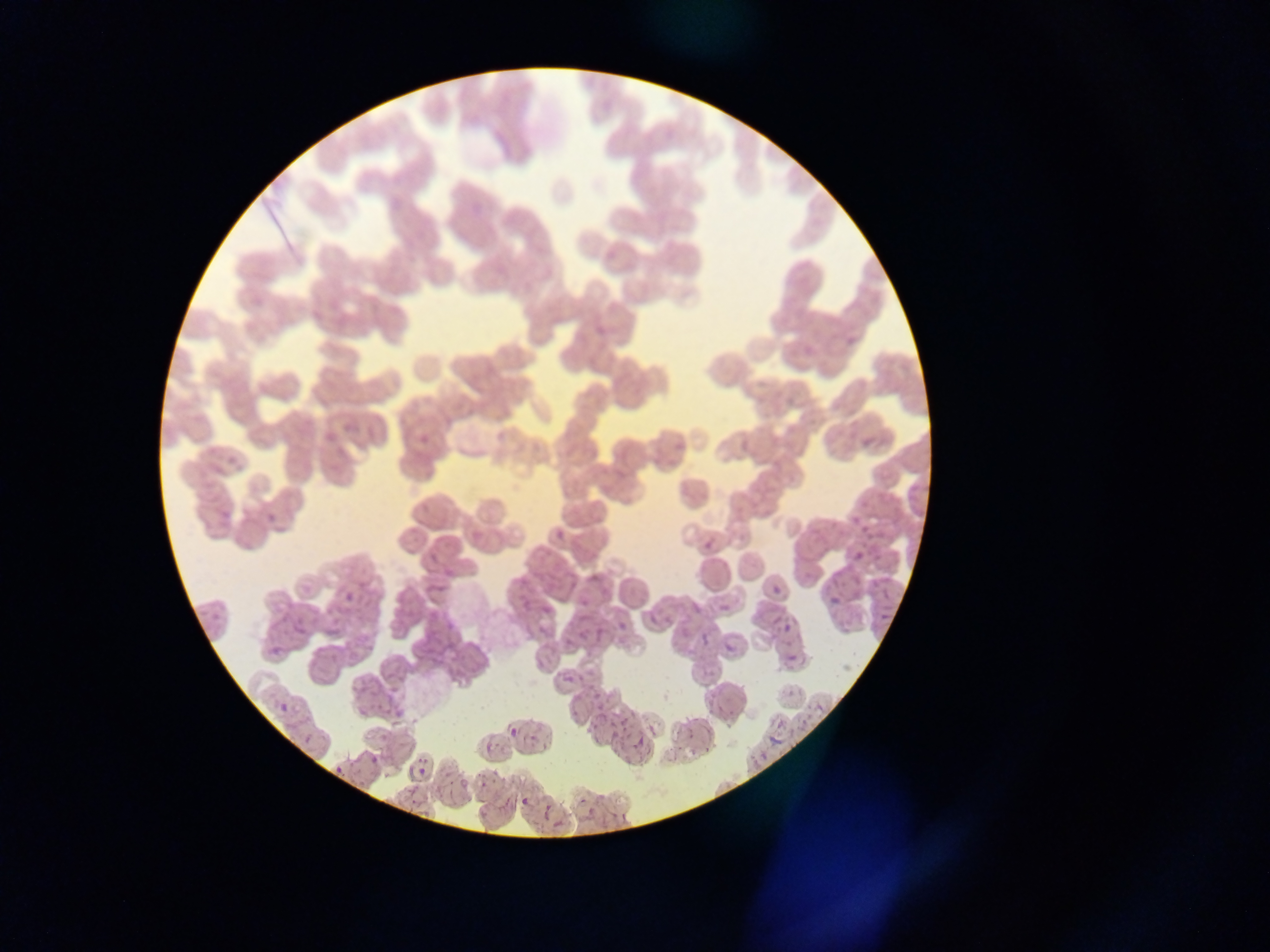

Approximate bounding boxes as left top right bottom in pixels.
Summary:
  - Malaria parasite locations: 419 433 428 443; 909 483 922 498; 857 491 871 517; 824 518 838 542; 862 521 876 536; 556 530 565 540; 705 540 713 548; 854 551 864 562; 848 570 862 586; 879 577 890 603; 772 585 781 594; 344 591 353 602; 829 596 840 605; 721 604 729 612; 687 605 703 625; 543 606 552 616; 642 606 664 628; 879 611 889 621; 428 613 452 641; 703 613 719 636; 293 621 308 637; 617 621 627 631; 784 622 792 634; 595 630 605 640; 722 638 736 652; 787 654 797 663; 564 674 573 683; 583 675 602 700; 707 690 726 716; 813 700 826 712; 278 701 288 712; 356 705 367 717; 595 708 606 727; 616 721 628 738; 682 724 699 738; 509 728 518 737; 631 736 641 758; 485 745 493 754; 371 755 380 765; 477 777 487 789; 520 797 528 806
  - Country: Ghana
  - Preparation: thin blood film
  - Image size: 1270×952 pixels
  - Field of view: single
  - Capture: mobile-phone photograph through a microscope